Assess for Plasmodium parasites.
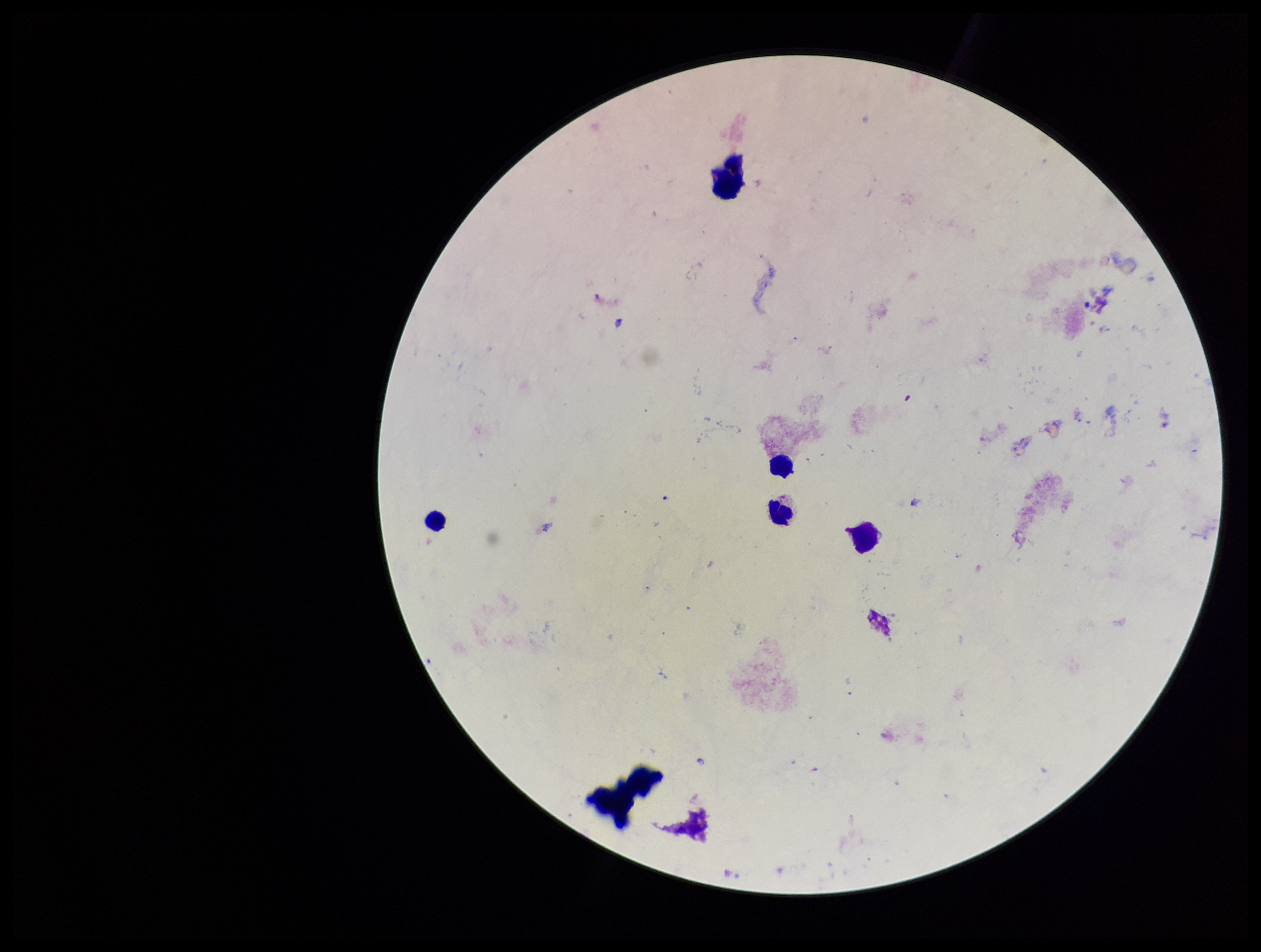
None seen.

patient malaria status = negative
stain = Giemsa
field of view = one from this slide
leukocyte count = 5
parasite count = 0
image size = 1261×952 pixels
preparation = thick blood smear
capture = smartphone photograph through the microscope eyepiece